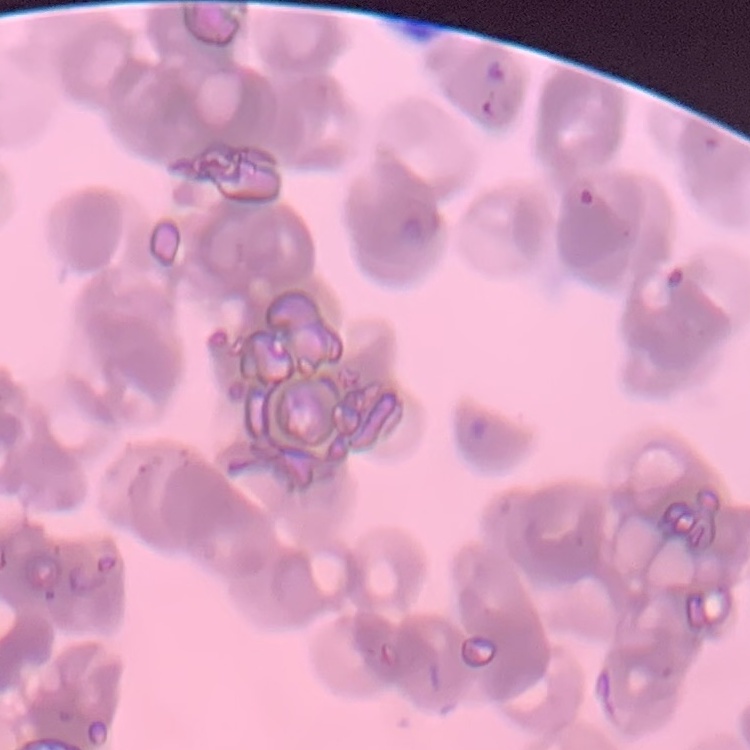
The erythrocytes exhibit rouleaux formation. Square crop of a larger photomicrograph. Stained with either Field's or Giemsa. Thin peripheral smear.